State which parasite is depicted.
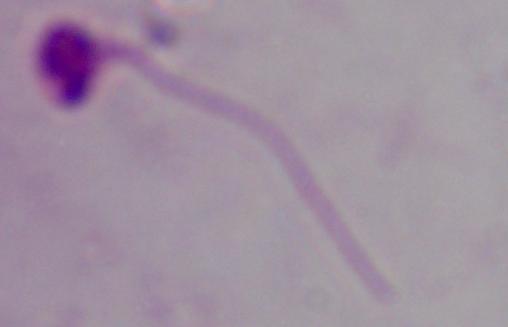
This is Leishmania.

Summary:
  - Modality: micrograph
  - Magnification: 1000x